Classify this cell by malaria status.
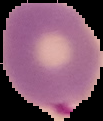
It is parasitized.

Segmented cell region on a black background. From a thin blood smear. Image is 103×121 pixels.